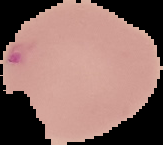 Image is 163×145 pixels. Result: Plasmodium parasites detected. Segmented cell region on a black background. From a thin blood film.